Name the blood parasite species.
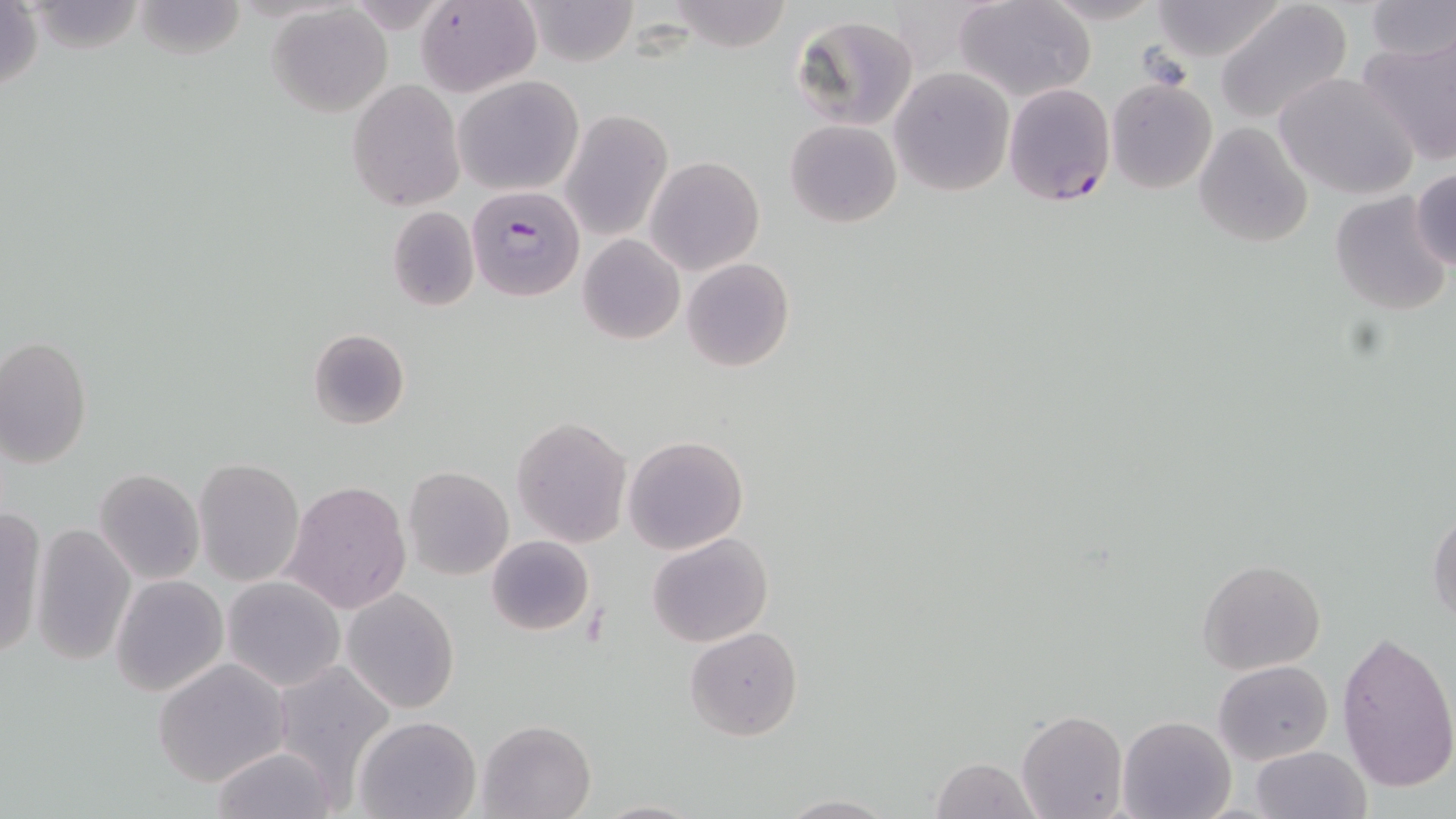

Plasmodium falciparum.

{
  "image_size": "1456×819 pixels",
  "preparation": "thin blood smear",
  "uninfected_red_blood_cell_locations_subset": "approximate bounding boxes as named x1/y1/x2/y2 corners in pixels: (x1=418, y1=0, x2=542, y2=97), (x1=520, y1=0, x2=639, y2=67), (x1=955, y1=0, x2=1097, y2=102), (x1=1040, y1=0, x2=1168, y2=26), (x1=1149, y1=0, x2=1291, y2=63), (x1=1363, y1=0, x2=1455, y2=63), (x1=665, y1=1, x2=794, y2=52), (x1=0, y1=2, x2=45, y2=97), (x1=131, y1=2, x2=247, y2=60), (x1=1215, y1=3, x2=1353, y2=128), (x1=267, y1=5, x2=394, y2=116), (x1=791, y1=16, x2=917, y2=131), (x1=1357, y1=33, x2=1456, y2=168), (x1=889, y1=67, x2=1016, y2=196), (x1=1273, y1=72, x2=1419, y2=200), (x1=453, y1=75, x2=584, y2=194), (x1=347, y1=79, x2=466, y2=211), (x1=1105, y1=79, x2=1217, y2=194), (x1=559, y1=109, x2=674, y2=243), (x1=785, y1=119, x2=902, y2=228), (x1=1193, y1=121, x2=1312, y2=247), (x1=646, y1=156, x2=764, y2=275), (x1=1412, y1=167, x2=1456, y2=272), (x1=1328, y1=188, x2=1452, y2=317), (x1=387, y1=207, x2=478, y2=310), (x1=578, y1=234, x2=685, y2=344), (x1=680, y1=258, x2=795, y2=372), (x1=307, y1=328, x2=410, y2=428), (x1=1, y1=335, x2=93, y2=469), (x1=512, y1=415, x2=633, y2=547), (x1=622, y1=435, x2=749, y2=556), (x1=193, y1=458, x2=306, y2=587), (x1=404, y1=466, x2=513, y2=579), (x1=95, y1=467, x2=205, y2=585), (x1=281, y1=480, x2=414, y2=615), (x1=1426, y1=506, x2=1456, y2=625), (x1=0, y1=510, x2=46, y2=662), (x1=30, y1=524, x2=135, y2=665), (x1=647, y1=532, x2=774, y2=647), (x1=487, y1=536, x2=594, y2=636), (x1=1197, y1=558, x2=1326, y2=674), (x1=111, y1=575, x2=227, y2=696), (x1=222, y1=577, x2=344, y2=691), (x1=342, y1=588, x2=461, y2=714), (x1=686, y1=626, x2=803, y2=741), (x1=1336, y1=631, x2=1456, y2=792), (x1=152, y1=657, x2=293, y2=786), (x1=270, y1=658, x2=399, y2=790), (x1=1213, y1=659, x2=1333, y2=766), (x1=1015, y1=710, x2=1127, y2=819), (x1=1117, y1=715, x2=1235, y2=818), (x1=355, y1=716, x2=481, y2=819), (x1=478, y1=718, x2=597, y2=819), (x1=208, y1=744, x2=338, y2=819), (x1=1251, y1=746, x2=1370, y2=819), (x1=931, y1=756, x2=1041, y2=818), (x1=776, y1=794, x2=897, y2=819), (x1=592, y1=798, x2=705, y2=818)",
  "field_of_view": "one of a larger specimen",
  "plasmodium_falciparum_infected_red_blood_cell_locations_subset": "approximate bounding boxes as named x1/y1/x2/y2 corners in pixels: (x1=1003, y1=82, x2=1116, y2=207)",
  "magnification": "1000x",
  "modality": "light microscopy",
  "platelet_locations": "approximate bounding boxes as named x1/y1/x2/y2 corners in pixels: (x1=1137, y1=46, x2=1192, y2=89)",
  "stain": "May-Grünwald-Giemsa"
}